Assess this cell for malaria.
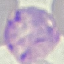

It is parasitized.

Thin blood film. Cell patch, automatically extracted from a larger field of view and resized to 64 × 64 pixels. Giemsa-stained preparation. Photographed with a smartphone camera at the microscope eyepiece.